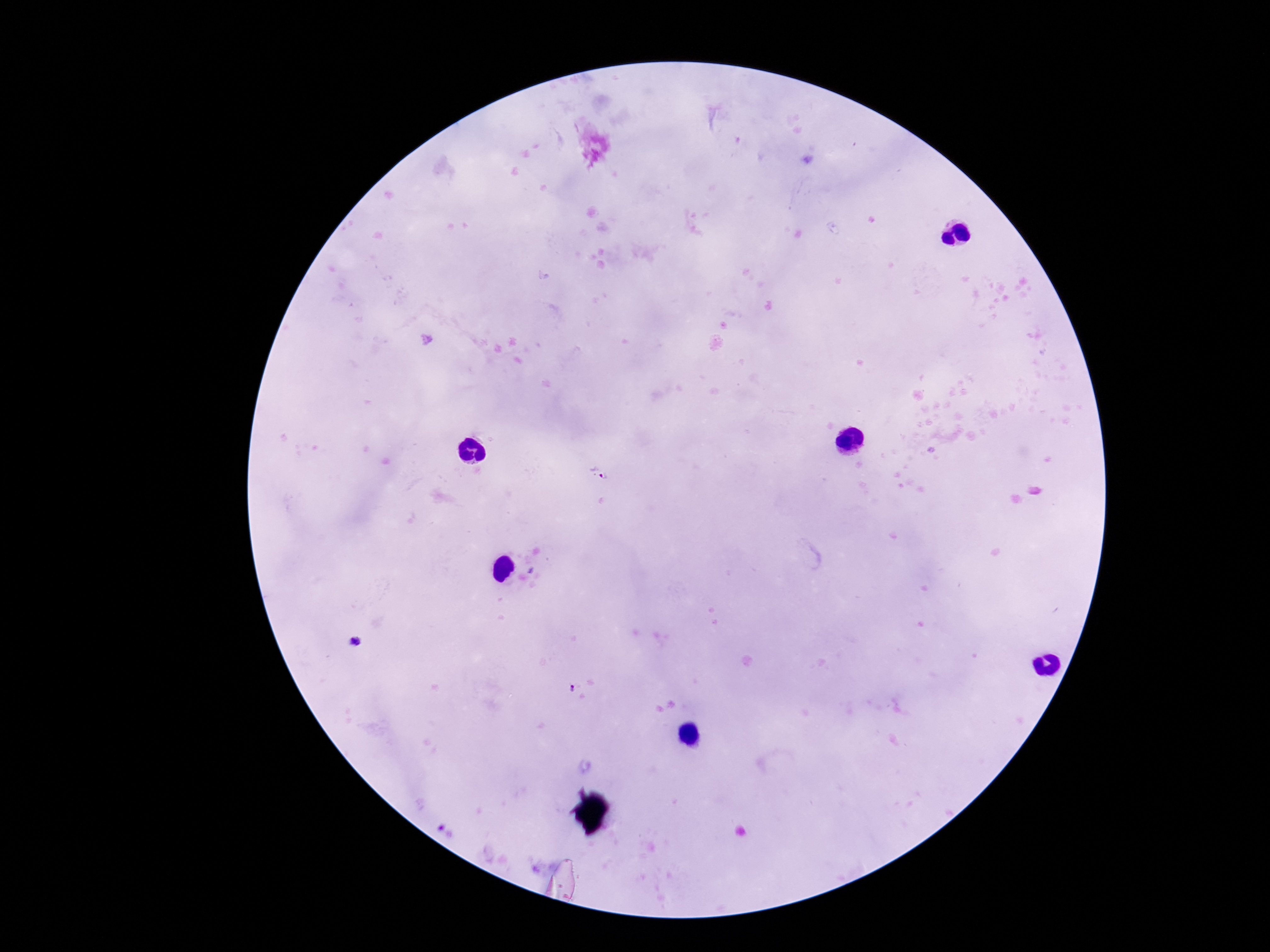

Approximate centers as [x, y] in pixels.
Summary:
  - Plasmodium parasite locations: [600, 474], [571, 689]
  - Patient malaria status: positive
  - Magnification: 100x
  - Stain: Giemsa
  - Image size: 1270×952 pixels
  - Capture: smartphone camera through the microscope eyepiece
  - Field of view: one from this slide
  - Preparation: thick peripheral-blood smear